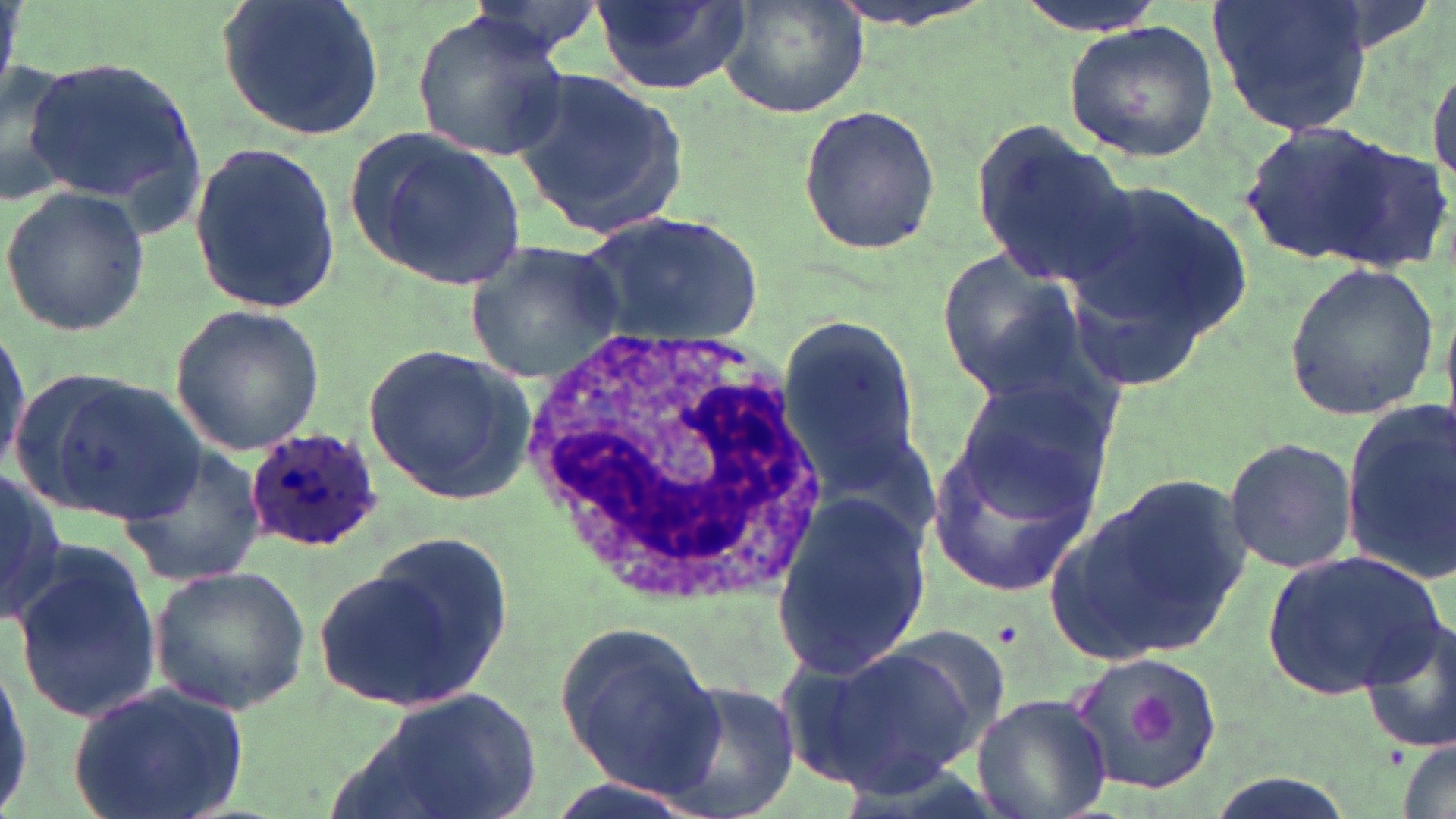
slide_level_diagnosis: Plasmodium ovale
magnification: 1000x
stain: May-Grünwald-Giemsa
white_blood_cell_locations: 'approximate bounding boxes as (x1,y1)-(x2,y2) corner pairs in pixels: (515,321)-(832,610)'
uninfected_red_blood_cell_locations: 'approximate bounding boxes as (x1,y1)-(x2,y2) corner pairs in pixels: (215,0)-(386,143), (590,0)-(749,95), (718,0)-(866,121), (824,0)-(1003,33), (1004,0)-(1169,36), (1207,0)-(1374,138), (409,9)-(568,163), (1063,20)-(1218,161), (1427,50)-(1456,195), (20,52)-(205,221), (0,59)-(81,206), (513,66)-(686,239), (797,102)-(942,256), (1239,118)-(1408,264), (968,120)-(1138,290), (349,124)-(527,294), (187,138)-(340,316), (1325,139)-(1453,271), (1058,173)-(1252,392), (2,187)-(151,335), (578,212)-(765,350), (466,240)-(628,381), (933,247)-(1092,400), (1281,261)-(1439,422), (169,305)-(326,458), (775,319)-(924,478), (0,325)-(31,473), (364,342)-(534,504), (948,380)-(1115,526), (1339,398)-(1456,584), (923,428)-(1103,593), (1223,436)-(1358,577), (115,443)-(268,586), (0,469)-(64,629), (1043,471)-(1255,668), (770,489)-(932,682), (7,535)-(162,725), (314,537)-(516,713), (1266,550)-(1445,695), (148,564)-(312,713), (1358,613)-(1454,755), (553,622)-(723,797), (866,623)-(1017,766), (798,639)-(982,794), (1064,651)-(1223,799), (0,652)-(32,819), (656,677)-(802,819), (63,680)-(252,819), (337,685)-(546,819), (972,693)-(1113,819), (1398,738)-(1454,819), (1201,770)-(1359,819)'
plasmodium_ovale_infected_red_blood_cell_locations: 'approximate bounding boxes as (x1,y1)-(x2,y2) corner pairs in pixels: (245,426)-(385,552)'
modality: light microscopy
platelet_locations: 'approximate bounding boxes as (x1,y1)-(x2,y2) corner pairs in pixels: (1127,687)-(1183,752)'
preparation: thin blood film
image_size: 1456×819 pixels
field_of_view: single